Locate every blood parasite and identify its species.
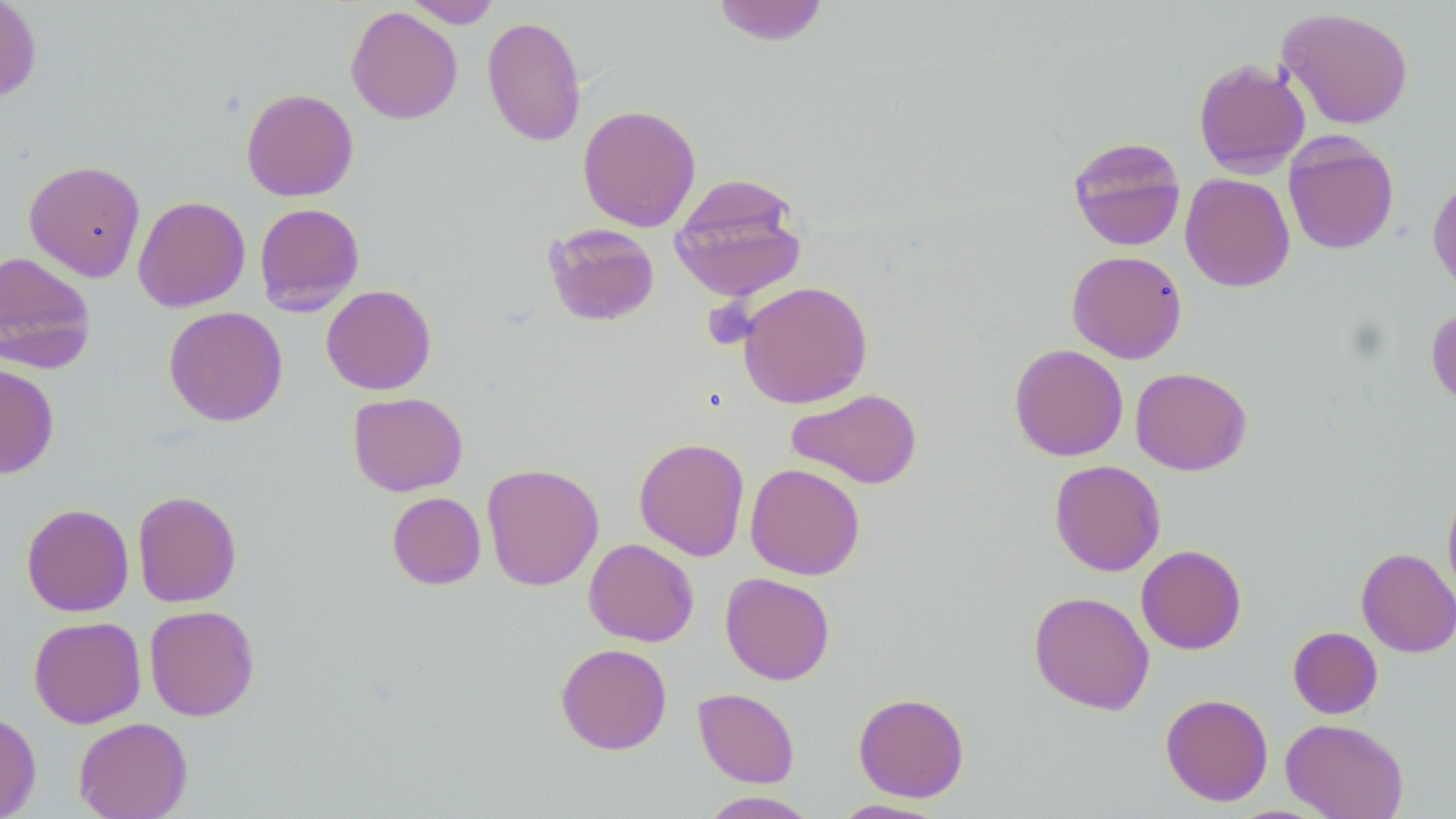
No blood parasites observed.

Approximate bounding boxes as (x1, y1, x2, y2) in pixels. Uninfected red blood cell locations: (0, 0, 42, 104), (404, 0, 501, 28), (711, 0, 829, 46), (346, 6, 463, 124), (1277, 6, 1414, 130), (482, 15, 586, 147), (1193, 58, 1311, 177), (241, 88, 358, 202), (577, 104, 701, 232), (1283, 133, 1399, 255), (1068, 135, 1186, 251), (24, 160, 146, 281), (1179, 173, 1295, 292), (670, 174, 807, 301), (1428, 177, 1456, 297), (133, 195, 250, 312), (254, 202, 365, 315), (543, 222, 660, 327), (1067, 250, 1187, 363), (0, 251, 96, 372), (738, 280, 873, 409), (321, 285, 437, 395), (1426, 303, 1456, 413), (164, 306, 288, 426), (1009, 343, 1128, 461), (0, 364, 60, 478), (1130, 367, 1252, 475), (786, 388, 923, 489), (348, 392, 468, 496), (633, 437, 750, 561), (1049, 460, 1166, 576), (481, 463, 604, 591), (745, 463, 864, 580), (1442, 481, 1456, 604), (132, 489, 242, 607), (387, 492, 486, 590), (21, 503, 134, 616), (583, 538, 699, 646), (1136, 544, 1247, 654), (1356, 547, 1456, 657), (720, 572, 836, 685), (1028, 591, 1154, 715), (144, 605, 260, 721), (29, 616, 146, 728), (1288, 626, 1383, 719), (556, 643, 672, 754), (693, 688, 800, 787), (853, 692, 969, 802), (1160, 693, 1273, 806), (0, 712, 41, 819), (74, 717, 193, 819), (1281, 718, 1409, 819), (698, 791, 820, 819), (831, 799, 952, 818). Slide-level diagnosis: no evidence of blood parasites. Optical microscopy. 1000x magnification. One field of a larger specimen. Image is 1456×819 pixels. Thin blood film. May-Grünwald-Giemsa stain.